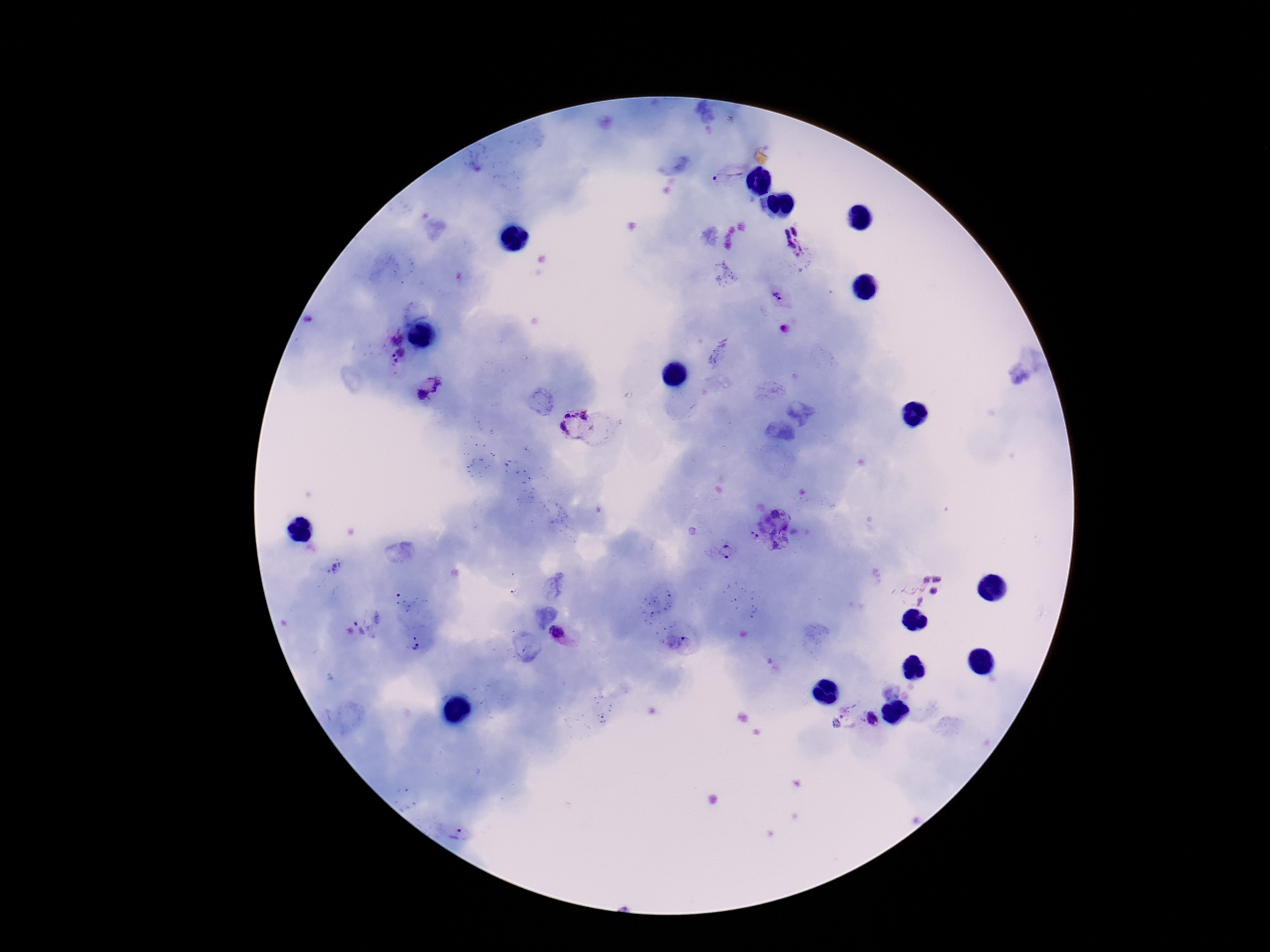
magnification: 100x
preparation: thick peripheral-blood smear
plasmodium_parasite_locations: 'approximate centers as (x, y) in pixels: (729, 178), (794, 242), (776, 296), (785, 329), (396, 340), (402, 353), (392, 355), (397, 361), (439, 383), (422, 395), (578, 425), (776, 514), (755, 535), (775, 545), (728, 551), (926, 579), (937, 579), (933, 591), (920, 601), (358, 628), (557, 632), (685, 640), (418, 643), (846, 709), (872, 718), (461, 835)'
capture: smartphone camera through the microscope eyepiece
field_of_view: single
patient_malaria_status: positive
stain: Giemsa
image_size: 1270×952 pixels